Point out malaria parasites and leukocytes.
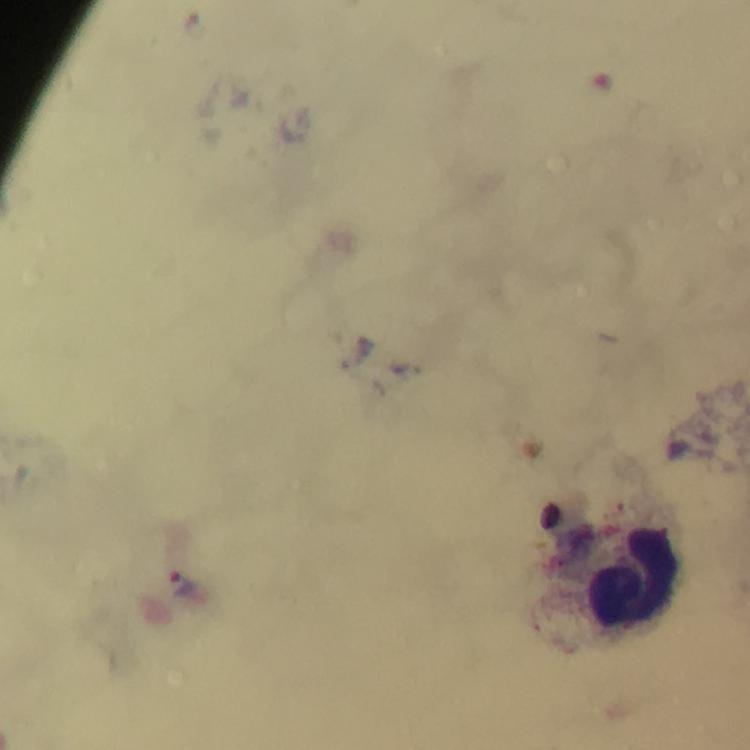
Approximate centers as (x, y) in pixels.
Malaria parasites: (183, 583).
Leukocytes: (635, 578).

immersion oil = used
image size = 750×750 pixels
magnification = 100x
stain = Giemsa
context = from a diagnostic examination for malaria
preparation = thick smear
cropped from = a single field of view
capture = smartphone camera through the microscope